Identify the blood parasite species.
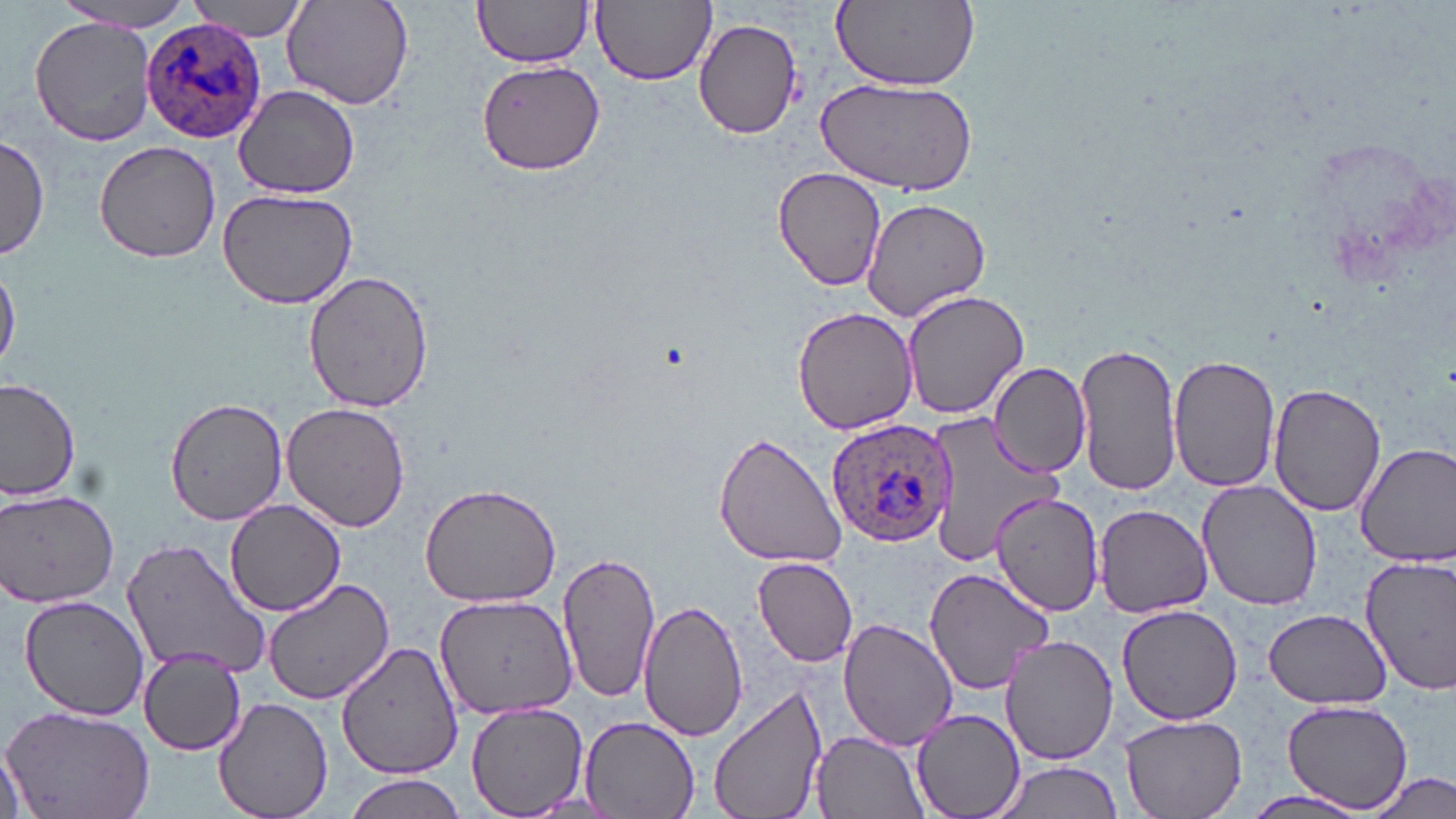
Plasmodium ovale.

{
  "stain": "May-Grünwald-Giemsa",
  "field_of_view": "single",
  "plasmodium_ovale_infected_red_blood_cell_locations": "approximate bounding boxes as [x1, y1, x2, y2] in pixels: [142, 18, 266, 143], [827, 417, 956, 547]",
  "magnification": "1000x",
  "uninfected_red_blood_cell_locations": "approximate bounding boxes as [x1, y1, x2, y2] in pixels: [472, 0, 595, 69], [591, 0, 717, 86], [831, 0, 978, 89], [187, 1, 311, 39], [282, 1, 416, 111], [47, 3, 193, 32], [30, 18, 156, 146], [693, 18, 802, 139], [477, 62, 604, 173], [817, 78, 977, 197], [234, 85, 360, 200], [0, 135, 50, 263], [93, 140, 223, 263], [771, 166, 887, 291], [214, 186, 362, 310], [862, 198, 991, 320], [0, 258, 21, 373], [302, 270, 436, 413], [902, 286, 1029, 420], [791, 306, 918, 434], [1073, 337, 1180, 496], [1168, 353, 1281, 493], [988, 363, 1093, 476], [0, 377, 81, 504], [1269, 383, 1386, 518], [164, 395, 290, 525], [281, 401, 411, 534], [918, 408, 1069, 569], [712, 431, 847, 569], [1353, 441, 1456, 568], [419, 481, 563, 608], [1198, 481, 1325, 610], [0, 486, 120, 609], [986, 490, 1103, 617], [225, 498, 345, 615], [1094, 505, 1212, 617], [121, 536, 272, 680], [557, 551, 661, 705], [1360, 555, 1456, 695], [752, 557, 858, 667], [922, 566, 1058, 694], [263, 577, 393, 704], [18, 592, 151, 720], [434, 592, 577, 721], [640, 597, 749, 743], [1119, 603, 1243, 725], [1265, 609, 1392, 708], [838, 617, 958, 751], [1001, 634, 1119, 764], [335, 641, 465, 780], [137, 650, 247, 755], [709, 683, 827, 819], [213, 697, 333, 819], [1282, 700, 1412, 812], [0, 702, 156, 819], [467, 703, 589, 817], [910, 708, 1027, 819], [1121, 713, 1250, 818], [579, 715, 702, 819], [811, 730, 931, 818], [0, 732, 35, 819], [990, 761, 1125, 819], [1365, 770, 1456, 819], [343, 775, 469, 819], [1238, 789, 1371, 818]",
  "modality": "light microscopy",
  "preparation": "thin blood film",
  "image_size": "1456×819 pixels"
}